State the preparation type.
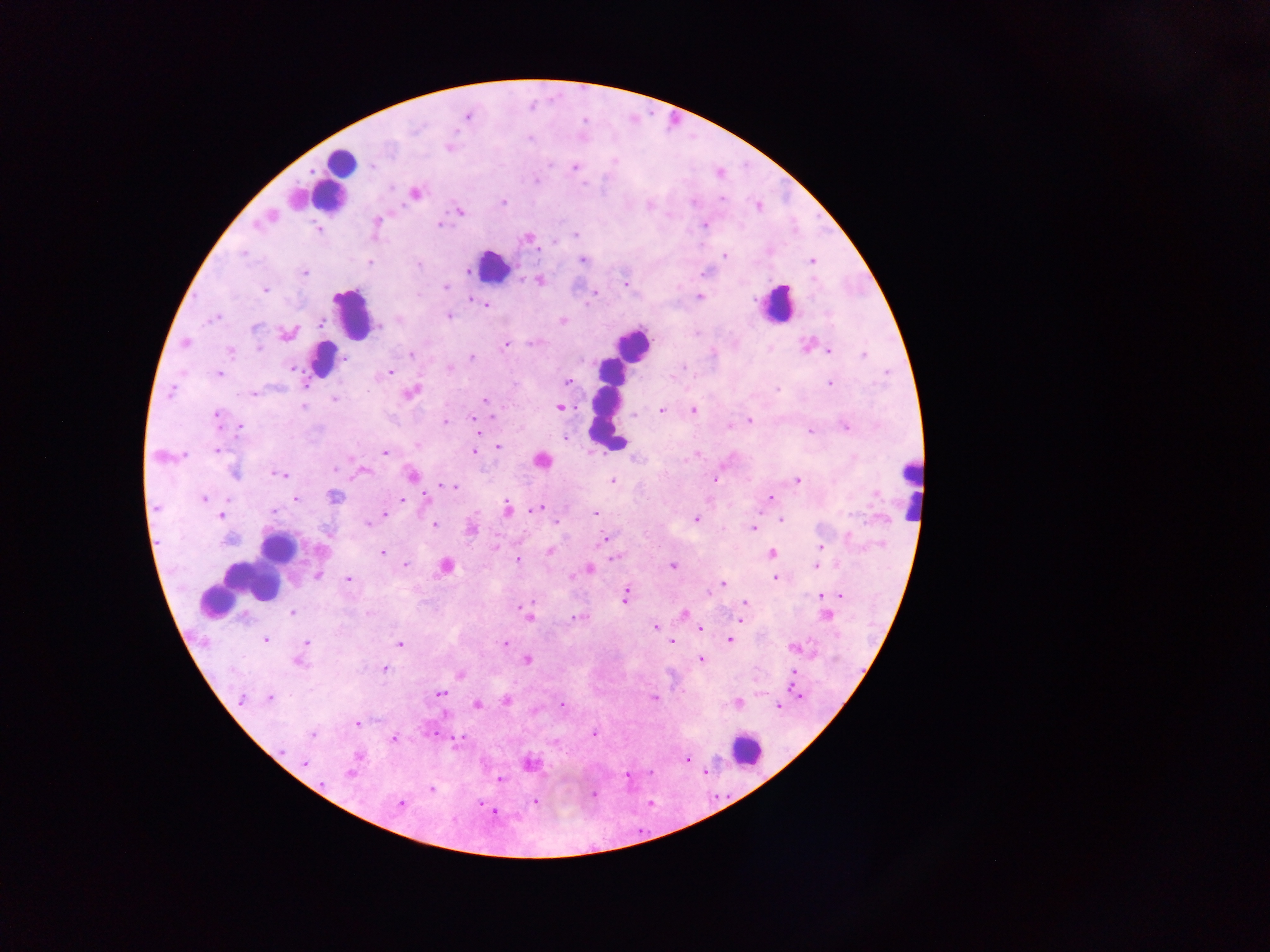

Thick blood film.

leukocyte_locations: 'approximate centers as x y in pixels: 341 162; 329 187; 493 265; 776 304; 352 313; 631 345; 322 357; 608 404; 910 487; 278 548; 254 579; 215 603; 747 750'
country: Ghana
capture: mobile-phone photograph through a microscope
image_size: 1270×952 pixels
field_of_view: single
malaria_parasite_locations: 'approximate centers as x y in pixels: 417 128; 530 138; 448 148; 615 160; 372 167; 574 167; 535 181; 584 184; 391 188; 415 193; 722 199; 503 202; 694 203; 648 206; 758 206; 459 212; 271 216; 377 220; 259 222; 440 224; 705 225; 318 229; 576 235; 528 238; 554 242; 243 254; 724 255; 582 260; 811 261; 370 263; 419 264; 466 271; 305 272; 539 280; 813 280; 624 284; 446 287; 265 290; 699 296; 471 299; 485 305; 449 316; 215 318; 563 320; 321 324; 255 327; 379 327; 287 334; 185 343; 531 343; 807 344; 505 346; 259 348; 829 351; 231 352; 411 355; 863 355; 471 357; 345 360; 684 367; 449 368; 291 369; 390 372; 219 373; 568 381; 829 383; 515 384; 777 388; 412 392; 169 393; 254 394; 335 399; 485 400; 303 407; 559 407; 693 410; 661 411; 217 415; 634 415; 491 417; 473 419; 445 421; 749 421; 729 425; 846 427; 241 429; 810 431; 565 438; 417 447; 498 447; 218 450; 384 452; 474 452; 185 454; 697 454; 541 461; 336 469; 361 471; 235 475; 281 475; 412 475; 716 480; 797 480; 612 481; 446 486; 452 486; 334 496; 426 497; 770 498; 204 499; 295 499; 402 500; 507 509; 536 509; 273 512; 385 513; 595 513; 221 516; 695 520; 555 521; 782 521; 368 524; 434 524; 752 529; 472 530; 849 537; 229 539; 603 541; 820 547; 496 548; 550 550; 383 553; 771 554; 614 558; 518 561; 404 565; 446 565; 671 566; 815 566; 590 570; 318 576; 775 577; 349 579; 722 583; 709 593; 822 595; 625 596; 840 596; 744 602; 531 603; 293 612; 684 615; 828 615; 529 617; 576 617; 741 621; 655 627; 700 628; 265 640; 729 640; 672 641; 307 642; 400 643; 505 644; 793 648; 528 659; 701 659; 299 664; 385 669; 793 673; 460 675; 441 693; 799 695; 270 698; 654 699; 241 700; 507 701; 738 703; 562 704; 477 705; 778 707; 357 723; 595 734; 313 735; 433 735; 393 739; 459 739; 687 758; 305 763; 530 763; 350 773; 627 776; 500 779; 322 783; 430 790; 593 794; 535 801; 399 803; 480 803; 495 812'